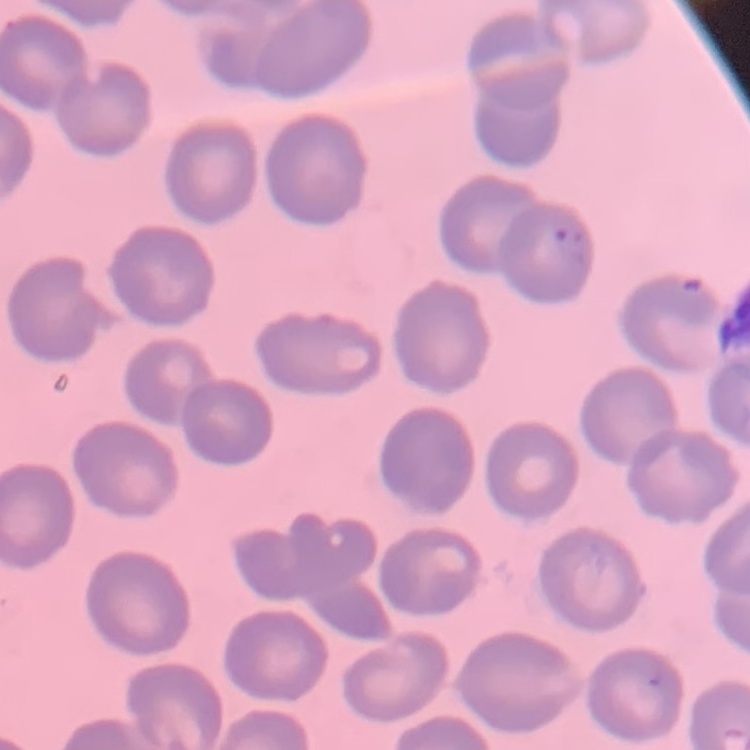
Summary:
  - Erythrocyte morphology: no rouleaux formation
  - Stain: Field's or Giemsa
  - Preparation: thin peripheral smear
  - Image type: square crop of a larger photomicrograph